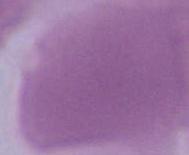

{
  "magnification": "1000x",
  "identification": "erythrocyte",
  "modality": "micrograph"
}